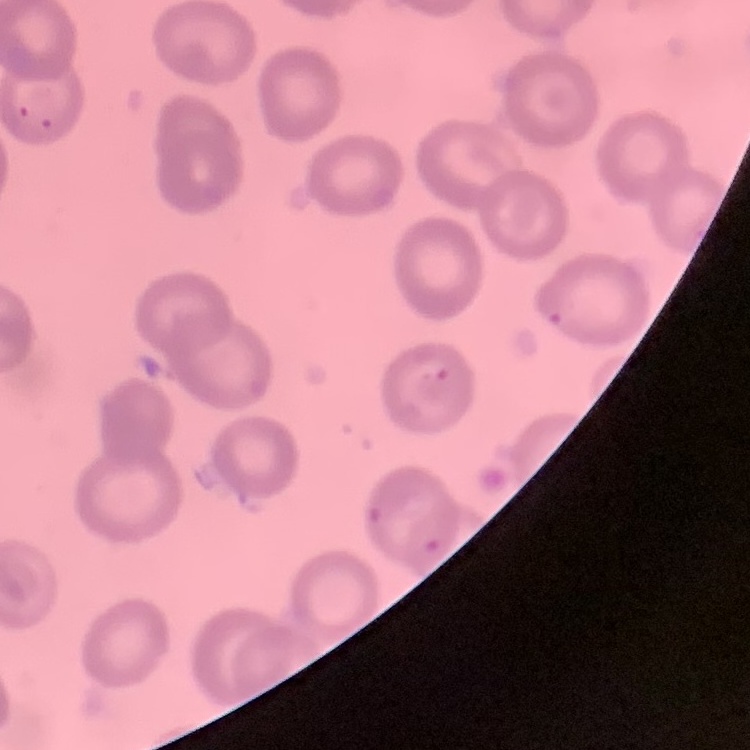

The red blood cells exhibit no rouleaux formation. Field's or Giemsa stain. Thin peripheral smear. One tile cut from a larger photomicrograph.